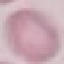
{
  "malaria_status": "uninfected",
  "preparation": "thin blood smear",
  "stain": "Giemsa",
  "capture": "smartphone camera at the microscope eyepiece",
  "image_type": "automatically extracted cell patch, resized to 64 × 64 pixels"
}